Classify this cell by malaria status.
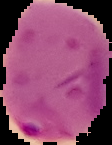
Parasitized.

Image is 112×145 pixels. The area outside the segmented cell region is set to black. From a thin blood smear.